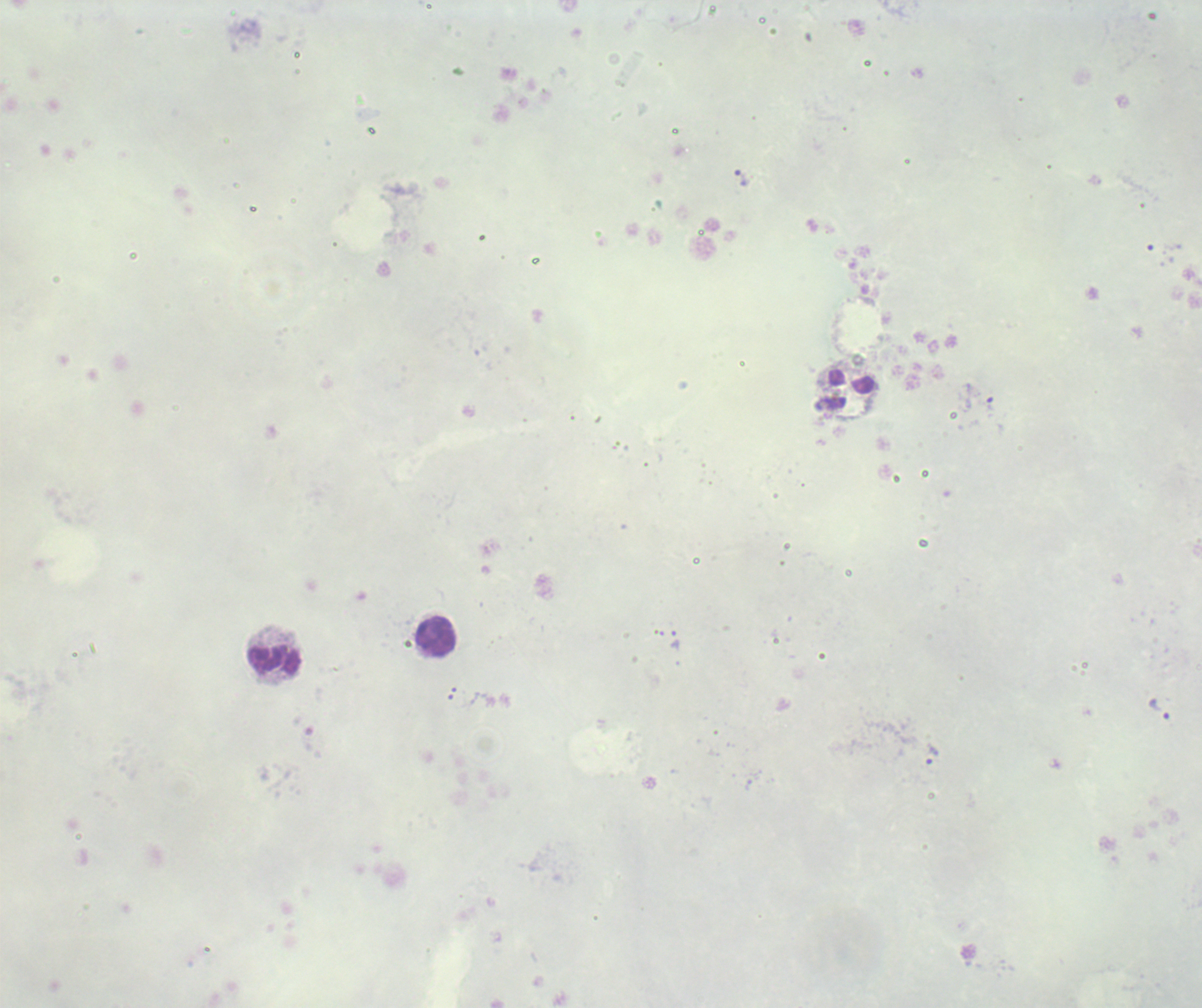

Approximate centers as [x, y] in pixels.
Summary:
  - Leukocyte locations: [437, 636], [275, 659]
  - Trophozoite locations: [742, 179], [830, 404], [674, 640], [1160, 710], [931, 755]
  - Magnification: 100x
  - Preparation: thick smear of blood
  - Image size: 1202×1008 pixels
  - Context: previously used in an actual diagnosis
  - Result: Plasmodium parasites identified
  - Field of view: single
  - Coloration quality: bad
  - Background quality: unsatisfactory
  - Stain: Romanowsky